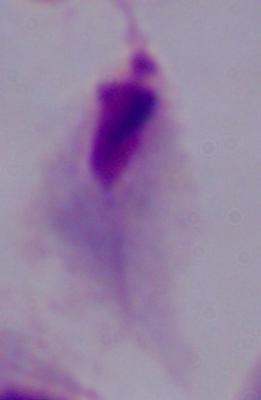
magnification = 1000x
identification = trichomonad
modality = micrograph